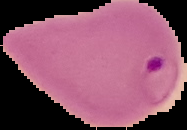

image size = 187×130 pixels
preparation = thin blood film
result = malaria parasites detected
image type = segmented cell region with the area outside set to black